Report the malaria status of this cell.
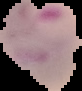

Parasitized.

image size = 82×91 pixels
preparation = thin blood smear
image type = cell region segmented out of the field of view; surrounding area masked to black